Report the malaria status of this cell.
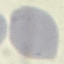

Uninfected.

image type = cell patch, automatically extracted from a larger field of view and resized to 64 × 64 pixels
stain = Giemsa
capture = smartphone camera at the microscope eyepiece
preparation = thin smear